Mark where platelets are.
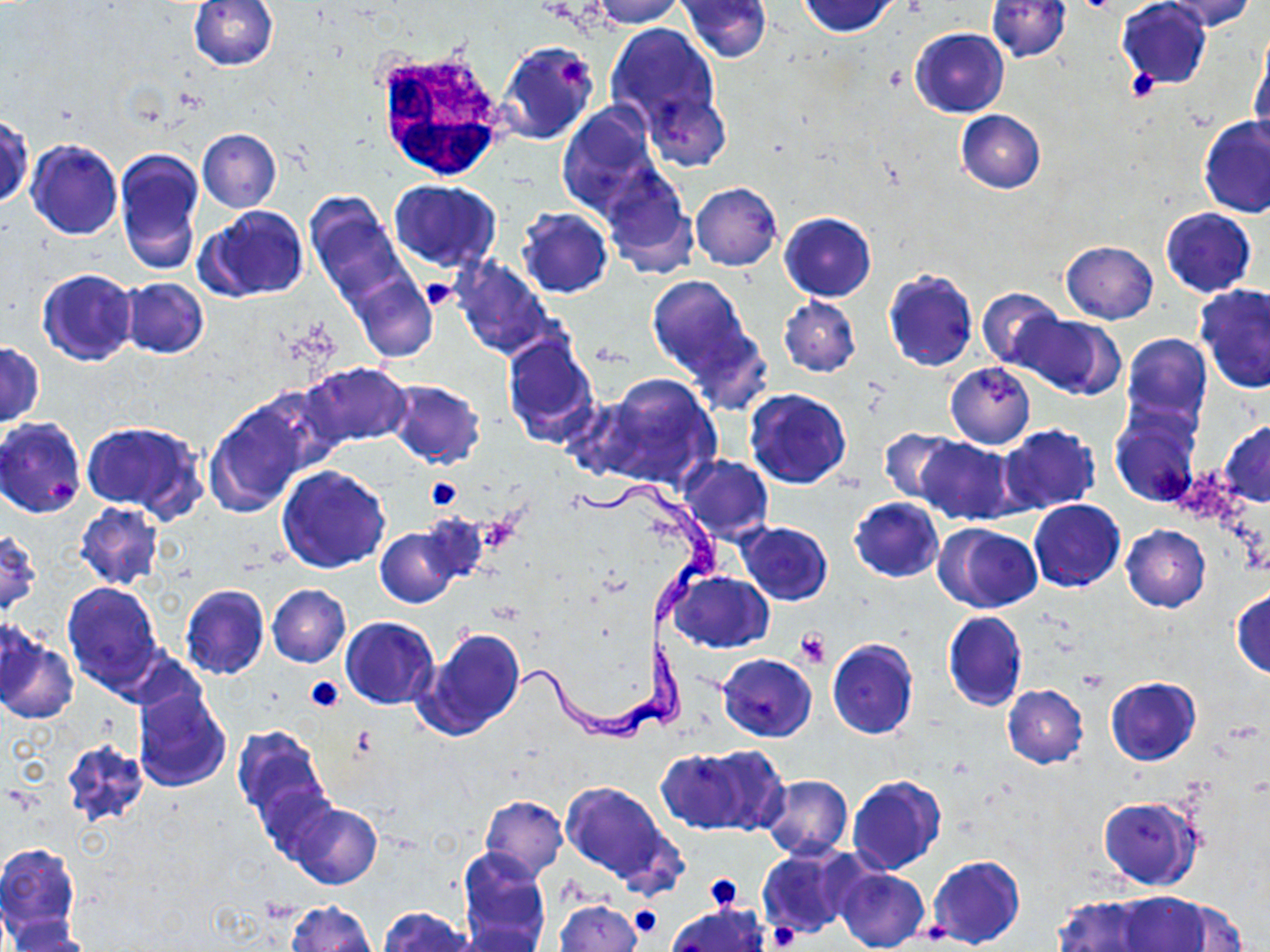
Approximate bounding boxes as (x1,y1)-(x2,y2) corner pairs in pixels.
Platelets: (557,53)-(589,91), (1127,68)-(1161,100), (421,279)-(456,311), (426,477)-(463,511), (476,515)-(521,554), (795,629)-(828,668), (305,677)-(343,712), (703,874)-(741,909), (630,906)-(661,937), (767,923)-(799,950), (915,923)-(952,946).

slide_level_diagnosis: Trypanosoma brucei
stain: May-Grünwald-Giemsa
preparation: thin blood smear
trypanosoma_brucei_locations: 'approximate bounding boxes as (x1,y1)-(x2,y2) corner pairs in pixels: (571,478)-(724,631), (513,632)-(699,749)'
uninfected_red_blood_cell_locations: 'approximate bounding boxes as (x1,y1)-(x2,y2) corner pairs in pixels: (187,0)-(279,71), (589,0)-(684,28), (678,0)-(771,62), (798,0)-(901,37), (988,0)-(1071,62), (1116,0)-(1213,88), (1160,0)-(1259,32), (605,23)-(720,129), (910,28)-(1009,118), (1250,34)-(1270,142), (498,40)-(598,145), (642,89)-(730,170), (556,103)-(662,217), (955,110)-(1046,193), (1,113)-(32,209), (1197,114)-(1270,219), (197,129)-(282,212), (26,139)-(122,239), (115,146)-(206,274), (600,167)-(696,276), (389,179)-(501,271), (691,182)-(782,271), (305,193)-(409,308), (197,204)-(309,302), (516,207)-(613,298), (1159,208)-(1257,297), (779,212)-(876,301), (1060,241)-(1158,324), (451,257)-(557,360), (37,268)-(138,366), (882,268)-(979,373), (350,271)-(436,363), (647,275)-(756,383), (119,278)-(208,359), (1195,284)-(1270,393), (977,287)-(1064,371), (779,296)-(860,376), (1016,314)-(1123,399), (500,331)-(600,446), (1121,334)-(1212,434), (0,342)-(44,429), (303,363)-(412,447), (945,364)-(1035,448), (582,374)-(721,494), (385,379)-(486,469), (744,388)-(853,490), (204,399)-(314,516), (1110,408)-(1200,507), (0,417)-(87,518), (82,421)-(207,519), (1220,421)-(1270,507), (998,425)-(1101,516), (878,428)-(962,507), (916,437)-(1018,524), (680,455)-(773,543), (277,465)-(390,573), (849,497)-(944,583), (1028,499)-(1125,592), (74,502)-(164,589), (941,513)-(1124,600), (737,521)-(833,605), (938,523)-(1043,613), (374,525)-(463,608), (1121,525)-(1210,612), (0,530)-(41,614), (669,571)-(774,653), (62,581)-(163,691), (179,584)-(270,680), (266,584)-(351,667), (1232,587)-(1270,679), (942,610)-(1028,711), (340,617)-(439,708), (413,626)-(527,741), (1,628)-(76,724), (657,630)-(682,734), (827,639)-(919,739), (718,653)-(817,742), (1106,676)-(1201,765), (1002,685)-(1087,768), (133,686)-(232,792), (232,724)-(332,828), (61,737)-(150,827), (654,747)-(767,833), (760,774)-(852,861), (847,775)-(946,875), (560,780)-(680,889), (480,795)-(568,878), (1099,796)-(1202,890), (285,801)-(382,890), (0,843)-(81,945), (757,843)-(863,940), (456,848)-(551,951), (927,855)-(1026,949), (835,868)-(929,952), (1112,891)-(1213,951), (1053,895)-(1158,952), (1153,896)-(1249,950), (555,899)-(642,952), (286,901)-(376,952), (665,903)-(770,952), (377,907)-(476,952), (7,926)-(97,952)'
white_blood_cell_locations: 'approximate bounding boxes as (x1,y1)-(x2,y2) corner pairs in pixels: (374,52)-(503,183)'
magnification: 1000x
image_size: 1270×952 pixels
modality: optical microscopy
field_of_view: single